Describe the morphology of the red blood cells.
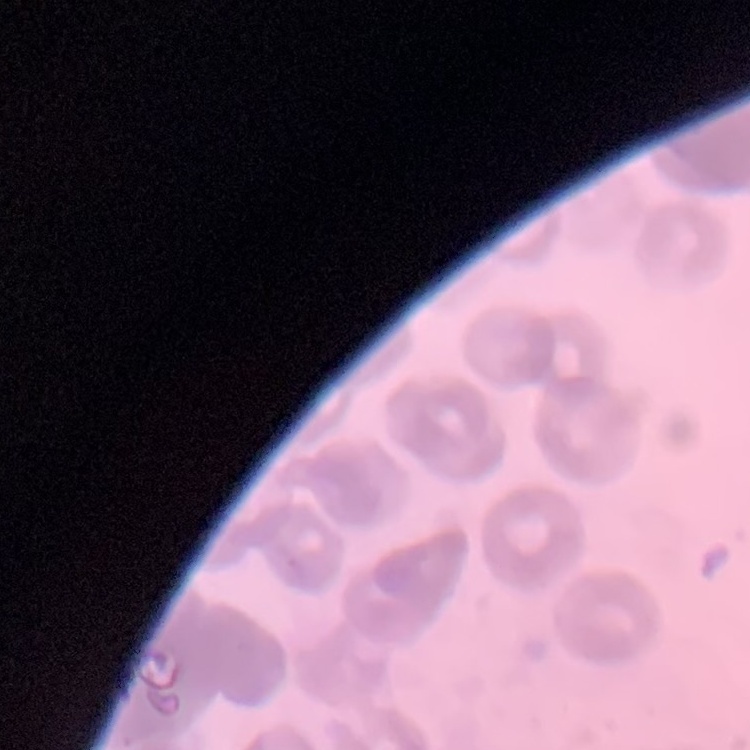
They show rouleaux formation.

Square crop of a larger photomicrograph. Thin peripheral smear. Field's or Giemsa stain.